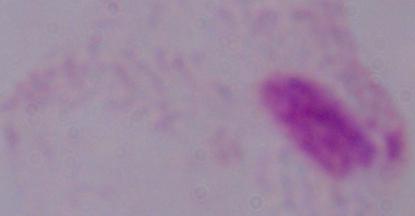
Summary:
  - Modality: micrograph
  - Magnification: 1000x
  - Identification: trichomonad